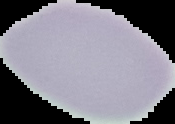

preparation = thin blood film
image type = segmented cell region on a black background
image size = 175×124 pixels
result = no malaria parasites detected